Describe the morphology of the red blood cells.
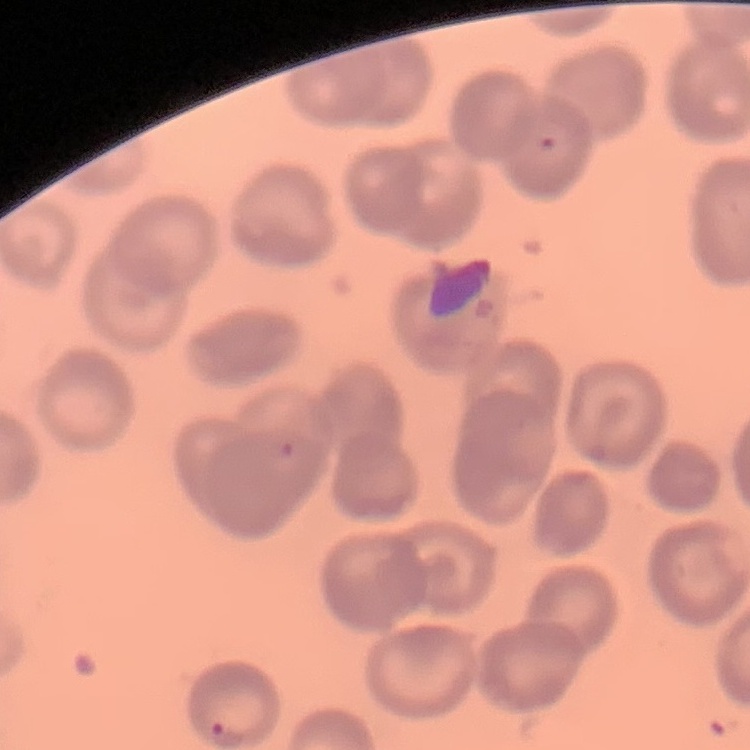

They show no rouleaux formation.

One tile cut from a larger photomicrograph. Stained with either Field's or Giemsa. Thin blood smear.